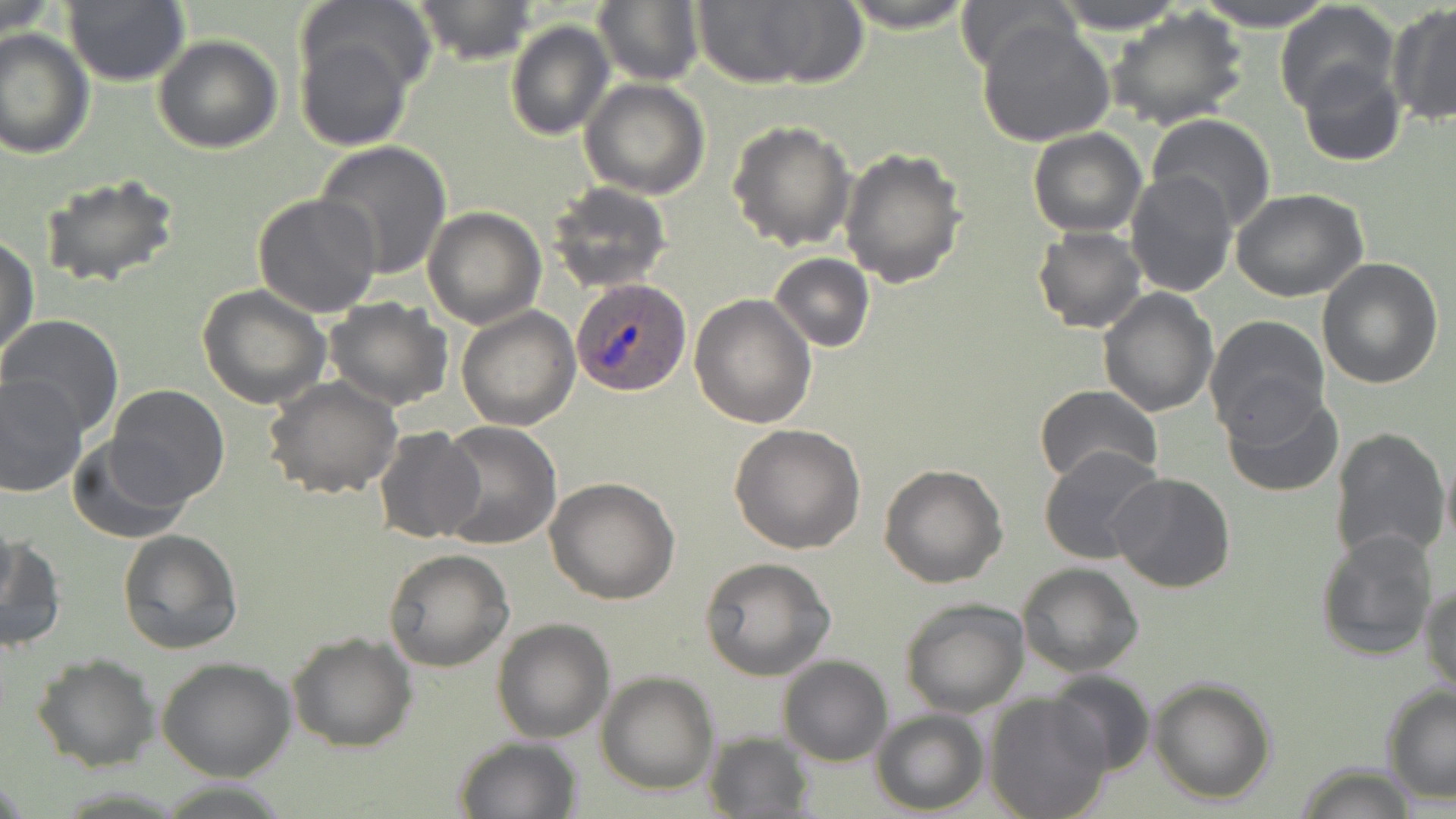
slide-level diagnosis = Plasmodium ovale
preparation = thin blood film
Plasmodium ovale-infected red blood cell locations = approximate bounding boxes as [x1, y1, x2, y2] in pixels: [572, 278, 693, 396]
image size = 1456×819 pixels
field of view = single
uninfected red blood cell locations = approximate bounding boxes as [x1, y1, x2, y2] in pixels: [0, 0, 60, 42], [413, 0, 537, 64], [593, 0, 705, 88], [691, 0, 862, 89], [839, 0, 977, 33], [1053, 0, 1188, 33], [1191, 0, 1339, 30], [954, 1, 1073, 73], [62, 2, 190, 87], [1275, 3, 1400, 118], [1386, 5, 1456, 126], [1106, 10, 1250, 131], [290, 16, 422, 152], [504, 19, 614, 141], [978, 19, 1115, 148], [0, 30, 94, 158], [152, 35, 284, 153], [1297, 60, 1406, 168], [579, 78, 711, 200], [1146, 114, 1276, 233], [727, 120, 855, 251], [1027, 128, 1146, 237], [314, 140, 453, 281], [839, 147, 967, 289], [1123, 170, 1238, 297], [38, 173, 181, 289], [547, 182, 672, 294], [1230, 188, 1369, 302], [252, 193, 383, 318], [423, 206, 546, 329], [1033, 226, 1147, 333], [0, 235, 38, 361], [769, 253, 873, 353], [1316, 257, 1444, 390], [196, 285, 331, 409], [1098, 286, 1218, 415], [690, 294, 818, 429], [321, 295, 453, 410], [456, 305, 581, 430], [0, 315, 125, 435], [1205, 315, 1329, 438], [0, 373, 88, 498], [265, 377, 404, 498], [107, 384, 230, 505], [1035, 384, 1164, 490], [1222, 389, 1344, 496], [435, 421, 562, 548], [729, 423, 865, 555], [1330, 425, 1450, 565], [372, 426, 486, 545], [68, 434, 193, 542], [1039, 446, 1168, 565], [1441, 446, 1455, 559], [878, 463, 1007, 588], [1109, 471, 1237, 592], [545, 477, 680, 605], [1313, 527, 1439, 662], [118, 528, 243, 654], [1, 532, 66, 653], [384, 548, 513, 672], [700, 557, 837, 681], [1016, 564, 1144, 677], [1421, 580, 1455, 695], [899, 597, 1029, 716], [492, 618, 614, 742], [287, 633, 417, 752], [30, 653, 159, 771], [778, 655, 893, 766], [156, 657, 297, 780], [596, 671, 719, 795], [1047, 671, 1156, 776], [1148, 677, 1278, 805], [1381, 685, 1456, 803], [983, 692, 1114, 819], [871, 709, 989, 815], [702, 732, 816, 819], [453, 736, 584, 819], [1292, 764, 1422, 818]
magnification = 1000x
stain = May-Grünwald-Giemsa
modality = optical microscopy